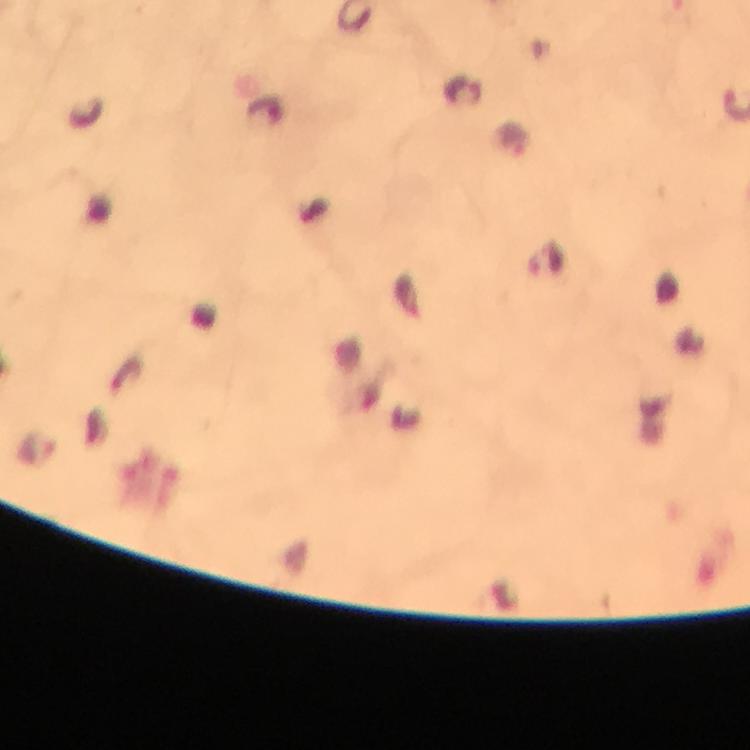 Approximate centers as (x, y) in pixels. Plasmodium parasite locations: (463, 90), (512, 139), (546, 261). Thick smear. Cropped region of a single field of view. From a malaria diagnostic workup. Smartphone photograph taken through a microscope. At 100x magnification. Image is 750×750 pixels. Giemsa-stained preparation. Immersion oil was used.